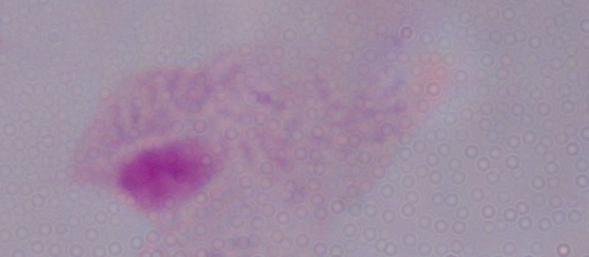
magnification: 1000x
modality: photomicrograph
identification: trichomonad